Give a bounding box for every parasitised red blood cell, every trophozoite, every gametocyte, every leukocyte, and every artifact (platelet-like body, stain precipitate, or debris).
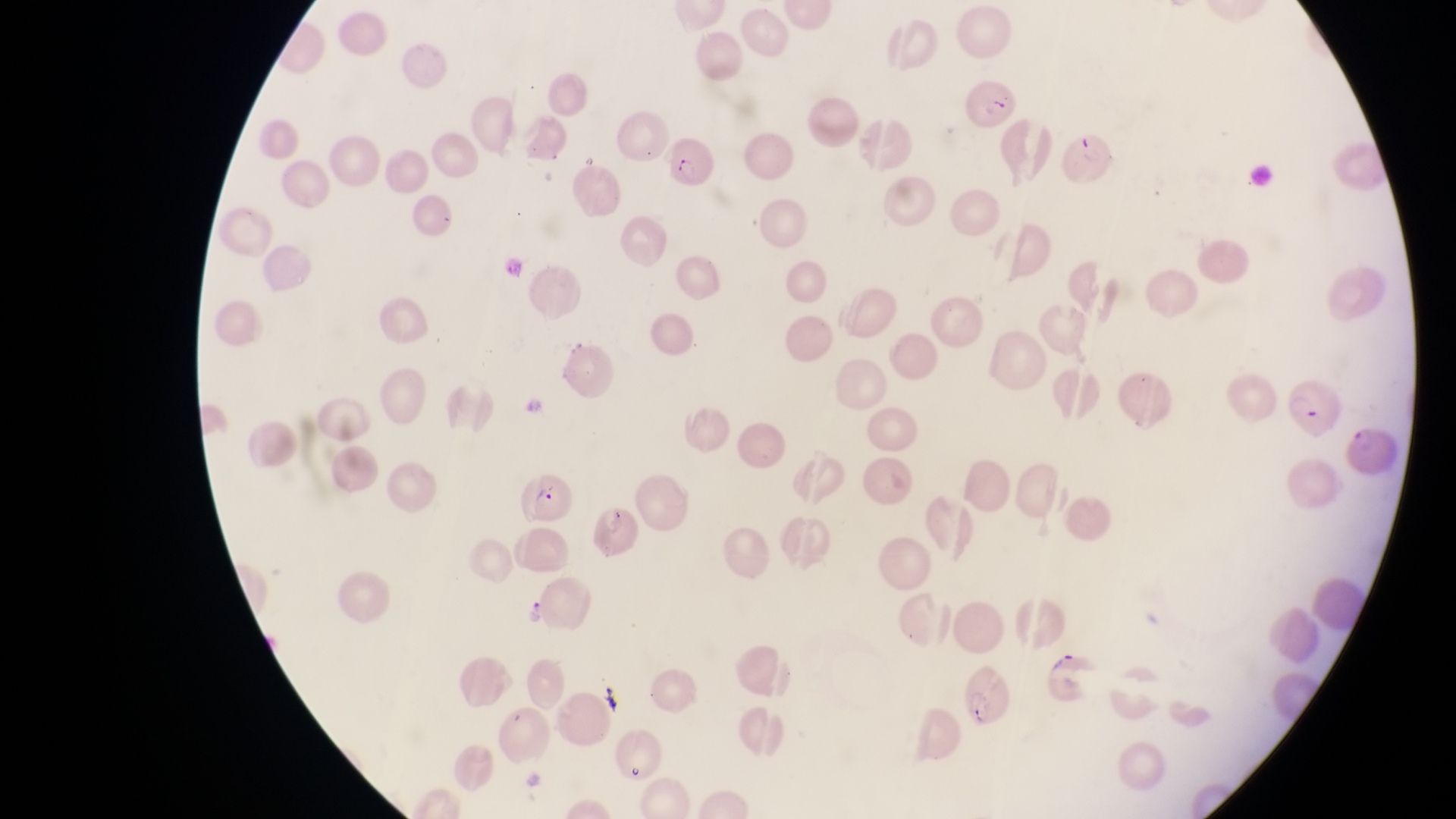

Approximate bounding boxes as [left, top, right, bottom] in pixels.
Parasitised red blood cells: [965, 79, 1017, 134], [1054, 129, 1117, 201], [667, 138, 720, 188], [1279, 375, 1339, 436], [518, 466, 577, 526], [957, 655, 1016, 728].
Trophozoites: [518, 591, 552, 634].
No leukocytes observed.

Summary:
  - Country: Uganda
  - Image size: 1456×819 pixels
  - Capture: smartphone photograph through the eyepiece of an Olympus CX-23 microscope
  - Magnification: 1000x
  - Preparation: thin blood film
  - Field of view: single